Identify the blood parasite species.
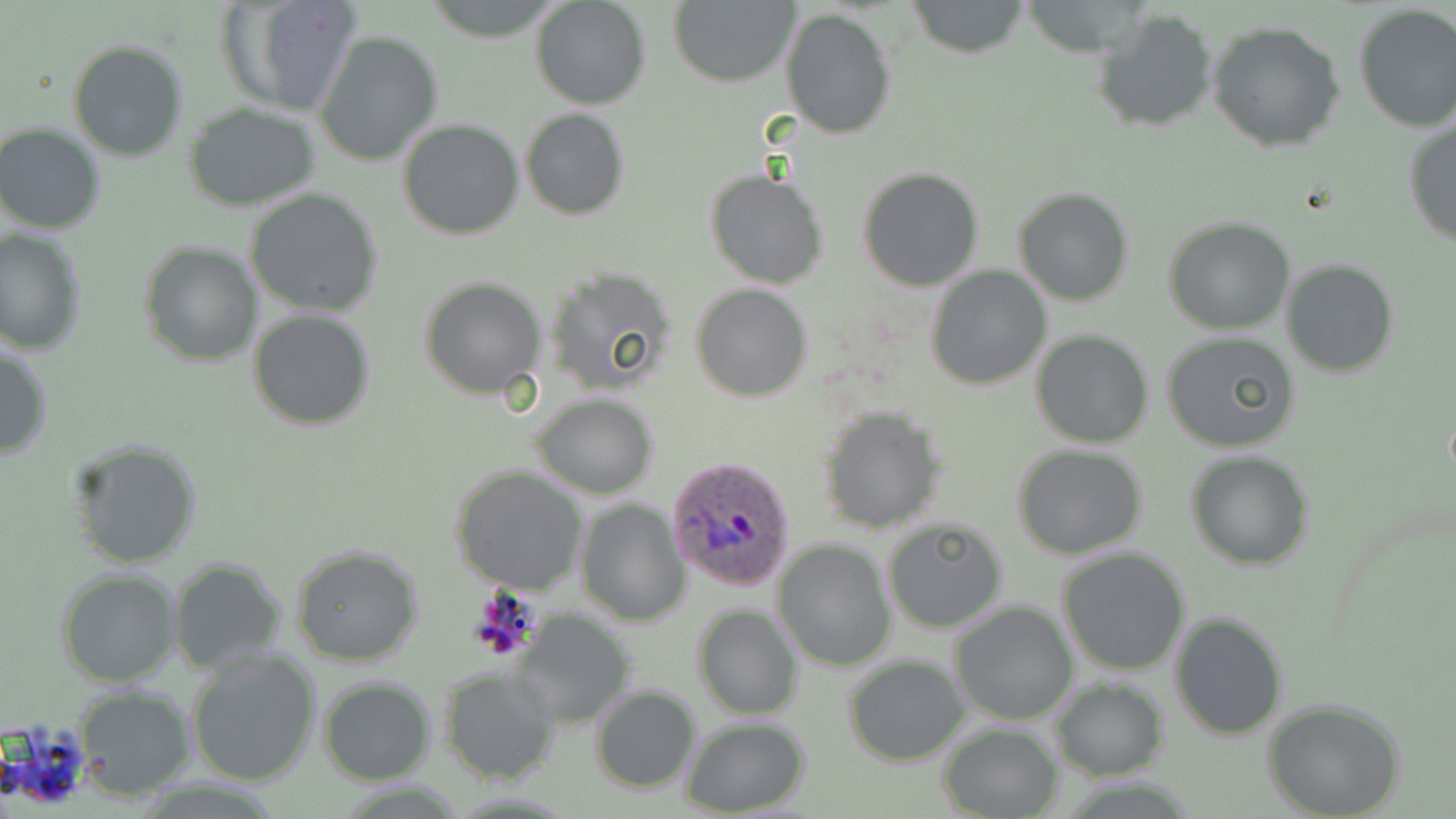
Plasmodium ovale.

Summary:
  - Coordinate format: approximate bounding boxes as (x1,y1)-(x2,y2) corner pairs in pixels
  - Uninfected red blood cell locations: (218,0)-(364,120), (419,0)-(564,40), (531,0)-(652,110), (669,0)-(800,87), (903,1)-(1031,59), (1352,4)-(1456,131), (1092,6)-(1220,134), (780,7)-(896,140), (1207,20)-(1349,153), (315,29)-(444,167), (67,39)-(189,162), (182,104)-(322,211), (519,108)-(630,219), (1403,117)-(1456,248), (397,118)-(525,240), (1,123)-(105,235), (858,167)-(985,292), (706,171)-(829,291), (1013,187)-(1135,307), (246,188)-(383,318), (1163,214)-(1296,334), (1,229)-(86,354), (140,241)-(262,367), (1281,258)-(1399,379), (925,266)-(1051,389), (542,268)-(677,395), (421,277)-(547,399), (690,282)-(814,402), (249,308)-(377,430), (1029,328)-(1155,448), (1160,331)-(1300,455), (0,339)-(53,461), (531,392)-(659,497), (818,406)-(946,533), (67,438)-(204,571), (1012,444)-(1148,560), (1186,450)-(1313,570), (450,464)-(588,595), (575,497)-(690,625), (882,518)-(1008,633), (772,540)-(894,671), (289,541)-(424,666), (1056,548)-(1190,678), (168,558)-(287,672), (56,568)-(183,687), (948,600)-(1078,725), (691,604)-(803,721), (513,610)-(637,729), (1169,613)-(1288,741), (186,647)-(323,787), (844,655)-(970,767), (439,668)-(560,785), (318,676)-(435,785), (1051,678)-(1169,780), (71,685)-(195,798), (590,685)-(701,794), (1261,697)-(1407,819), (682,717)-(811,816), (940,722)-(1062,819)
  - Plasmodium ovale-infected red blood cell locations: (668,456)-(798,592)
  - Preparation: thin blood smear
  - Field of view: single
  - Stain: May-Grünwald-Giemsa
  - Modality: optical microscopy
  - Image size: 1456×819 pixels
  - Magnification: 1000x